Give the extent of all uninfected red blood cells.
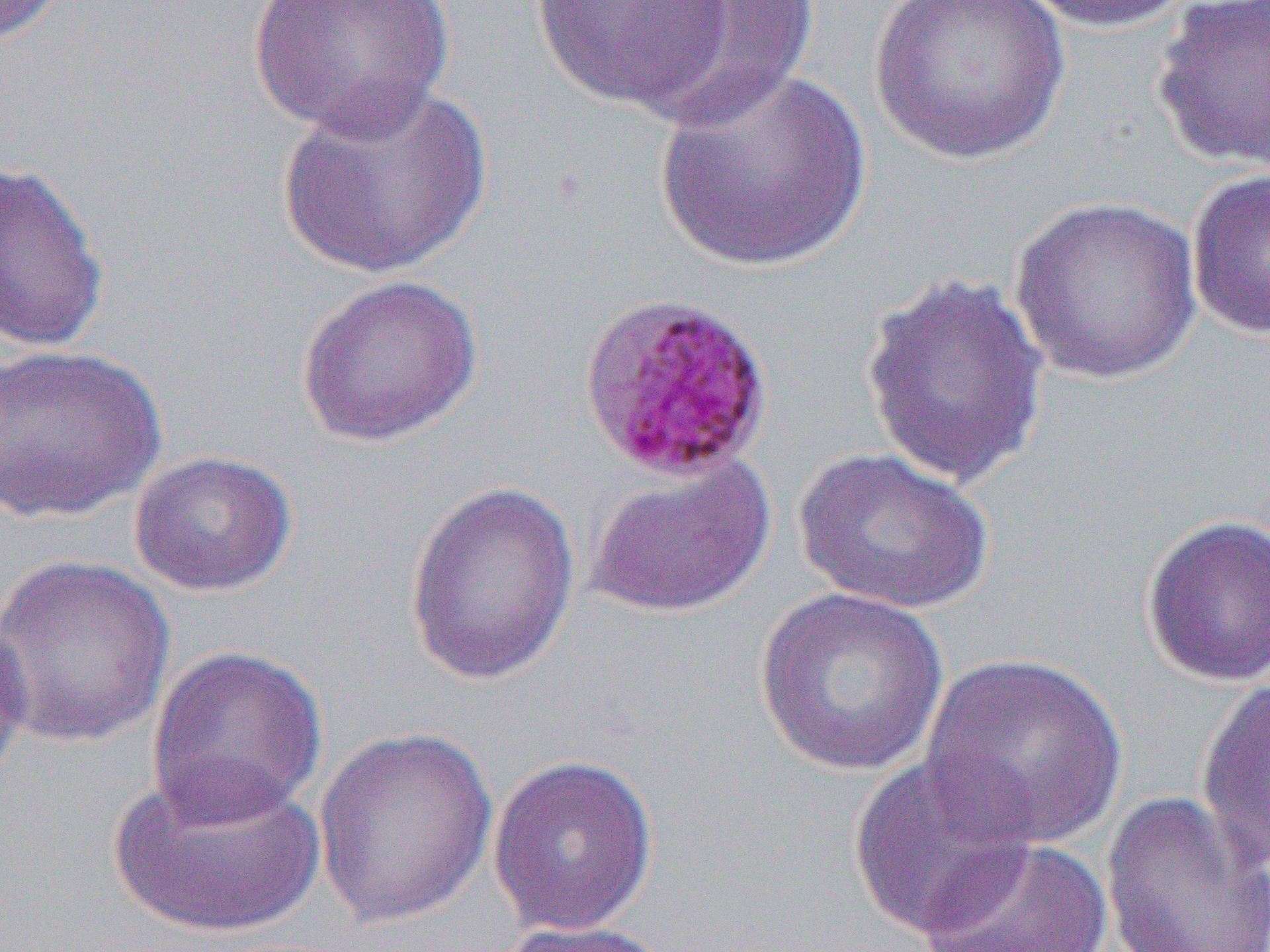
Approximate bounding boxes as named x1/y1/x2/y2 corners in pixels.
Uninfected red blood cells: (x1=0, y1=0, x2=73, y2=48), (x1=248, y1=0, x2=457, y2=139), (x1=530, y1=0, x2=733, y2=111), (x1=629, y1=0, x2=821, y2=130), (x1=866, y1=0, x2=1072, y2=168), (x1=1016, y1=0, x2=1196, y2=34), (x1=1152, y1=1, x2=1270, y2=173), (x1=654, y1=68, x2=873, y2=273), (x1=277, y1=80, x2=494, y2=280), (x1=0, y1=159, x2=110, y2=354), (x1=1185, y1=167, x2=1270, y2=341), (x1=1008, y1=196, x2=1203, y2=386), (x1=859, y1=271, x2=1051, y2=490), (x1=294, y1=273, x2=484, y2=449), (x1=0, y1=343, x2=167, y2=524), (x1=793, y1=447, x2=996, y2=615), (x1=128, y1=450, x2=297, y2=597), (x1=585, y1=452, x2=777, y2=620), (x1=403, y1=479, x2=581, y2=688), (x1=1139, y1=513, x2=1270, y2=688), (x1=0, y1=553, x2=176, y2=750), (x1=754, y1=587, x2=950, y2=777), (x1=0, y1=609, x2=35, y2=798), (x1=145, y1=644, x2=328, y2=828), (x1=919, y1=651, x2=1129, y2=851), (x1=1194, y1=676, x2=1270, y2=874), (x1=312, y1=725, x2=498, y2=930), (x1=846, y1=750, x2=1040, y2=940), (x1=487, y1=754, x2=659, y2=937), (x1=106, y1=761, x2=326, y2=941), (x1=1100, y1=790, x2=1270, y2=952), (x1=917, y1=835, x2=1115, y2=951), (x1=495, y1=919, x2=680, y2=951).

Summary:
  - Plasmodium malariae-infected red blood cell locations: (x1=576, y1=292, x2=775, y2=485)
  - Slide-level diagnosis: Plasmodium malariae
  - Preparation: thin blood film
  - Image size: 1270×952 pixels
  - Magnification: 1000x
  - Field of view: one of a larger specimen
  - Modality: light microscopy